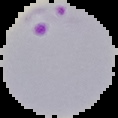

Summary:
  - Image size: 118×118 pixels
  - Preparation: thin blood film
  - Image type: segmented cell region with the area outside set to black
  - Malaria status: parasitized